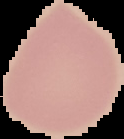
Summary:
  - Malaria status: uninfected
  - Image type: segmented cell region on a black background
  - Image size: 124×139 pixels
  - Preparation: thin blood film